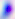
Photomicrograph. Toxoplasma gondii is shown. Captured at 400x magnification.